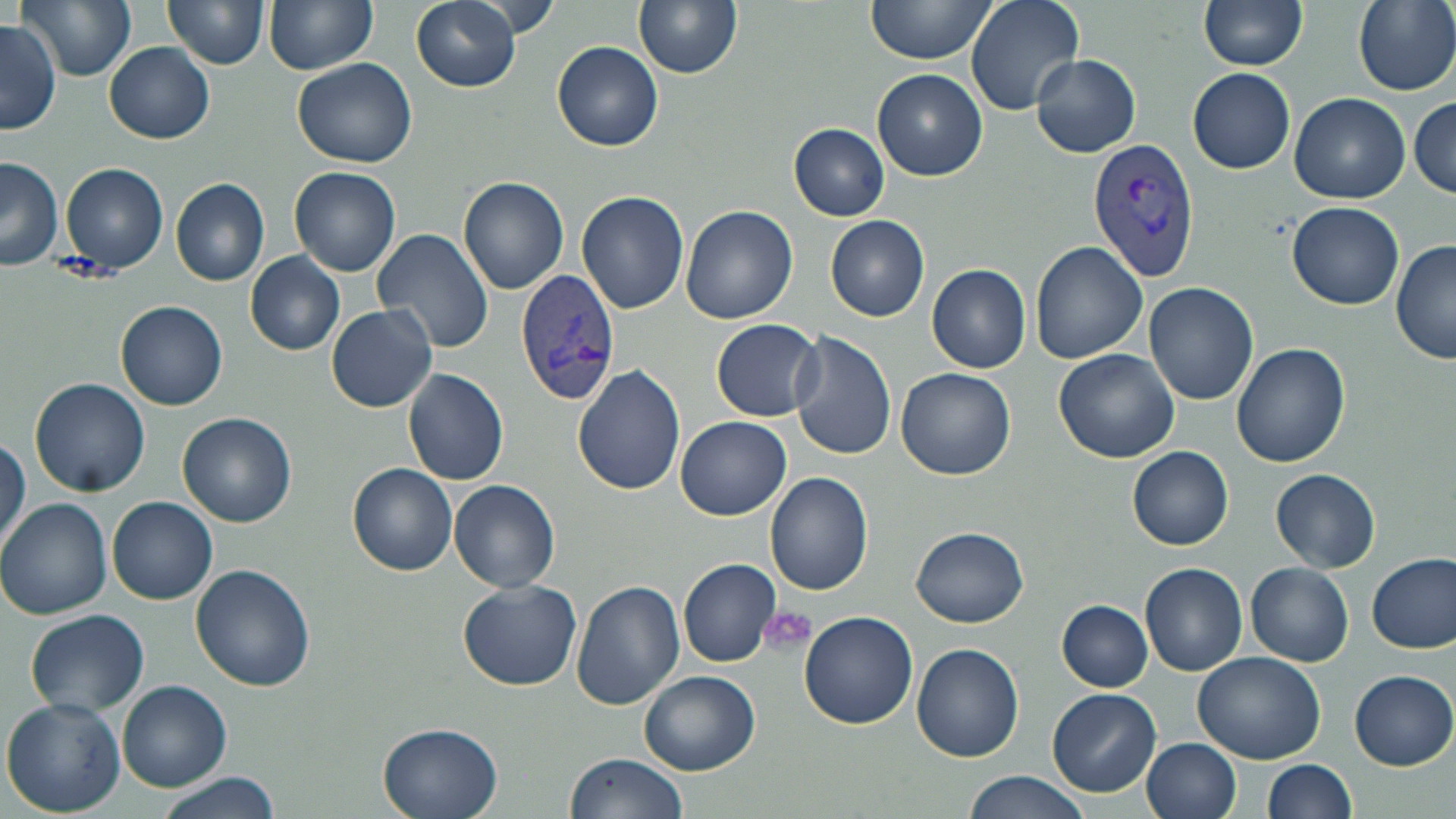
{
  "slide_level_diagnosis": "Plasmodium vivax",
  "image_size": "1456×819 pixels",
  "field_of_view": "single",
  "uninfected_red_blood_cell_locations": "approximate bounding boxes as (x1,y1)-(x2,y2) corner pairs in pixels: (18,0)-(136,81), (163,0)-(268,70), (263,0)-(377,74), (411,0)-(521,92), (634,0)-(741,78), (865,0)-(996,64), (966,0)-(1083,113), (1198,0)-(1307,71), (1354,0)-(1456,95), (0,20)-(60,133), (552,40)-(663,151), (104,41)-(216,144), (1030,53)-(1140,159), (292,58)-(417,167), (1188,67)-(1296,174), (873,69)-(987,181), (1288,94)-(1410,204), (1409,96)-(1455,196), (790,124)-(889,220), (0,158)-(63,270), (60,163)-(169,276), (288,166)-(402,276), (458,176)-(569,294), (171,177)-(270,287), (575,190)-(689,315), (1288,201)-(1403,310), (681,203)-(797,324), (826,215)-(930,321), (372,227)-(494,353), (1031,240)-(1148,364), (1391,240)-(1456,366), (245,253)-(346,357), (928,264)-(1031,373), (1144,281)-(1259,405), (116,301)-(227,410), (326,305)-(437,412), (711,319)-(823,422), (790,331)-(900,463), (1232,342)-(1351,468), (1053,348)-(1180,462), (572,367)-(685,498), (896,367)-(1016,479), (403,369)-(509,486), (29,377)-(149,498), (179,413)-(297,528), (676,416)-(792,521), (0,433)-(30,557), (1126,445)-(1234,548), (346,463)-(459,575), (1270,470)-(1381,571), (765,472)-(873,595), (451,479)-(560,593), (108,496)-(219,605), (0,498)-(112,619), (911,525)-(1028,627), (1368,554)-(1456,652), (678,557)-(781,667), (1140,562)-(1247,676), (1246,563)-(1353,666), (191,566)-(314,692), (570,578)-(685,710), (458,581)-(582,690), (1056,599)-(1153,691), (24,609)-(150,718), (798,610)-(921,728), (913,643)-(1025,762), (1194,651)-(1326,764), (1350,671)-(1455,769), (640,672)-(761,776), (117,681)-(231,791), (1047,689)-(1160,796), (1,697)-(126,819), (377,723)-(504,819), (1143,737)-(1242,819), (565,752)-(689,819), (1263,759)-(1357,819), (964,770)-(1093,819), (154,773)-(281,817)",
  "preparation": "thin blood smear",
  "stain": "May-Grünwald-Giemsa",
  "magnification": "1000x",
  "plasmodium_vivax_infected_red_blood_cell_locations": "approximate bounding boxes as (x1,y1)-(x2,y2) corner pairs in pixels: (1089,136)-(1200,284), (515,268)-(621,404)",
  "platelet_locations": "approximate bounding boxes as (x1,y1)-(x2,y2) corner pairs in pixels: (758,606)-(817,657)",
  "modality": "light microscopy"
}